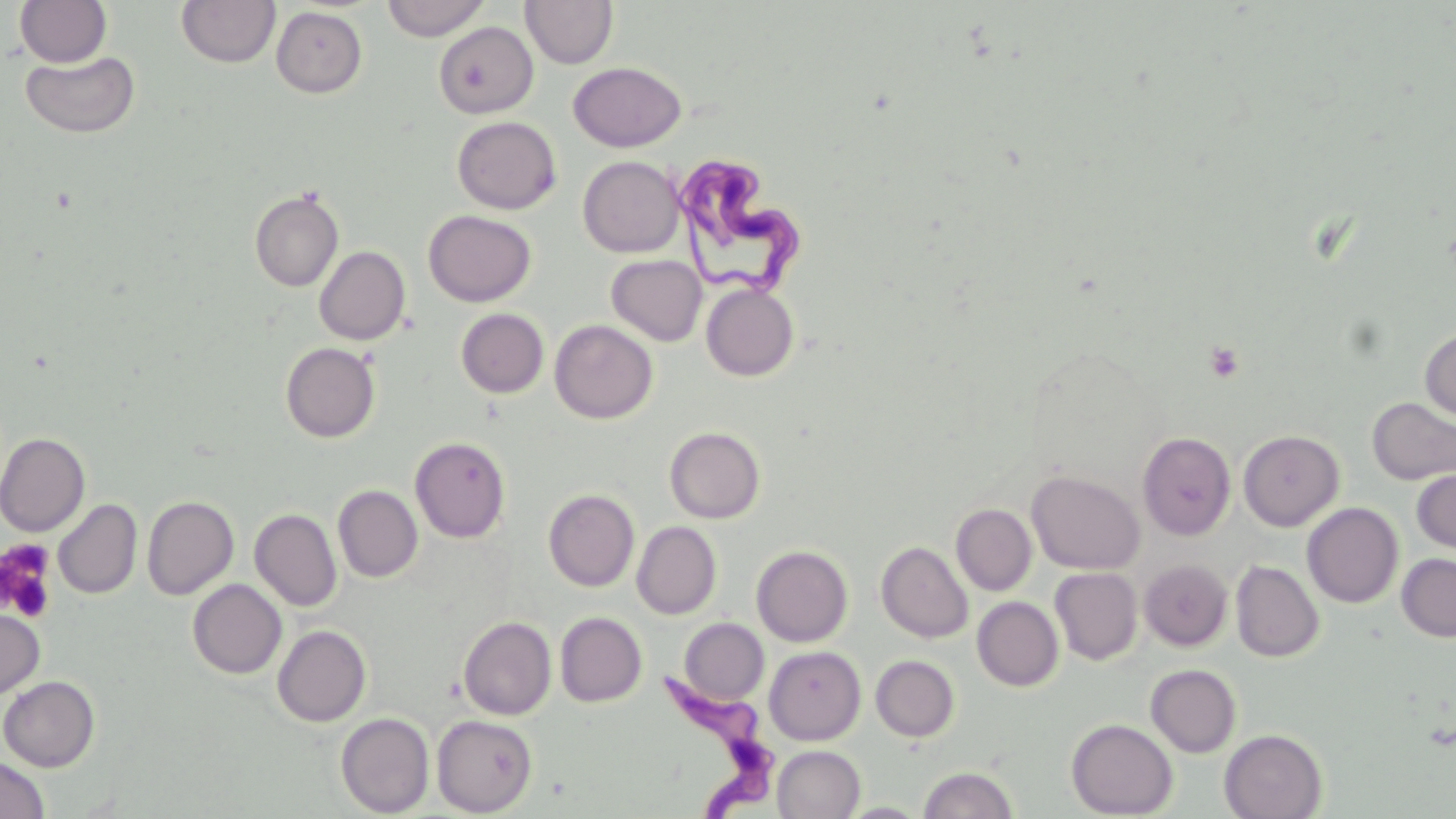
Summary:
  - Coordinate format: approximate bounding boxes as (x1,y1)-(x2,y2) corner pairs in pixels
  - Uninfected red blood cell locations: (15,0)-(112,67), (176,0)-(281,68), (381,0)-(490,41), (520,0)-(618,69), (271,6)-(367,98), (434,21)-(538,118), (19,51)-(141,138), (568,61)-(687,152), (452,116)-(561,214), (578,156)-(684,258), (249,188)-(344,292), (423,210)-(536,306), (314,246)-(410,345), (606,255)-(707,346), (701,282)-(798,381), (455,308)-(549,398), (549,319)-(657,424), (1419,325)-(1456,424), (280,342)-(380,443), (1366,396)-(1456,486), (665,427)-(765,523), (1238,430)-(1344,531), (0,432)-(90,536), (1137,432)-(1236,540), (410,436)-(510,542), (1411,469)-(1456,554), (1027,470)-(1144,574), (333,485)-(422,582), (543,489)-(639,592), (142,495)-(239,600), (53,499)-(142,599), (1301,502)-(1404,607), (951,504)-(1037,595), (250,508)-(342,612), (632,521)-(722,619), (876,541)-(973,643), (751,545)-(852,646), (1397,553)-(1456,642), (1139,559)-(1232,650), (1231,560)-(1324,662), (1049,567)-(1142,664), (188,579)-(286,679), (972,597)-(1064,691), (0,604)-(45,699), (555,612)-(647,707), (458,616)-(556,720), (679,619)-(769,704), (272,625)-(371,727), (764,645)-(866,745), (871,655)-(960,741), (1145,664)-(1242,757), (0,676)-(100,771), (336,713)-(434,817), (432,715)-(538,816), (1066,719)-(1178,818), (1220,729)-(1327,819), (772,745)-(865,819), (0,756)-(50,819), (918,766)-(1018,819), (840,802)-(929,818)
  - Trypanosoma brucei locations: (673,152)-(805,297), (657,670)-(791,814)
  - Platelet locations: (1204,340)-(1245,384), (1,540)-(57,623)
  - Slide-level diagnosis: Trypanosoma brucei
  - Preparation: thin blood film
  - Field of view: single
  - Image size: 1456×819 pixels
  - Modality: light microscopy
  - Stain: May-Grünwald-Giemsa
  - Magnification: 1000x